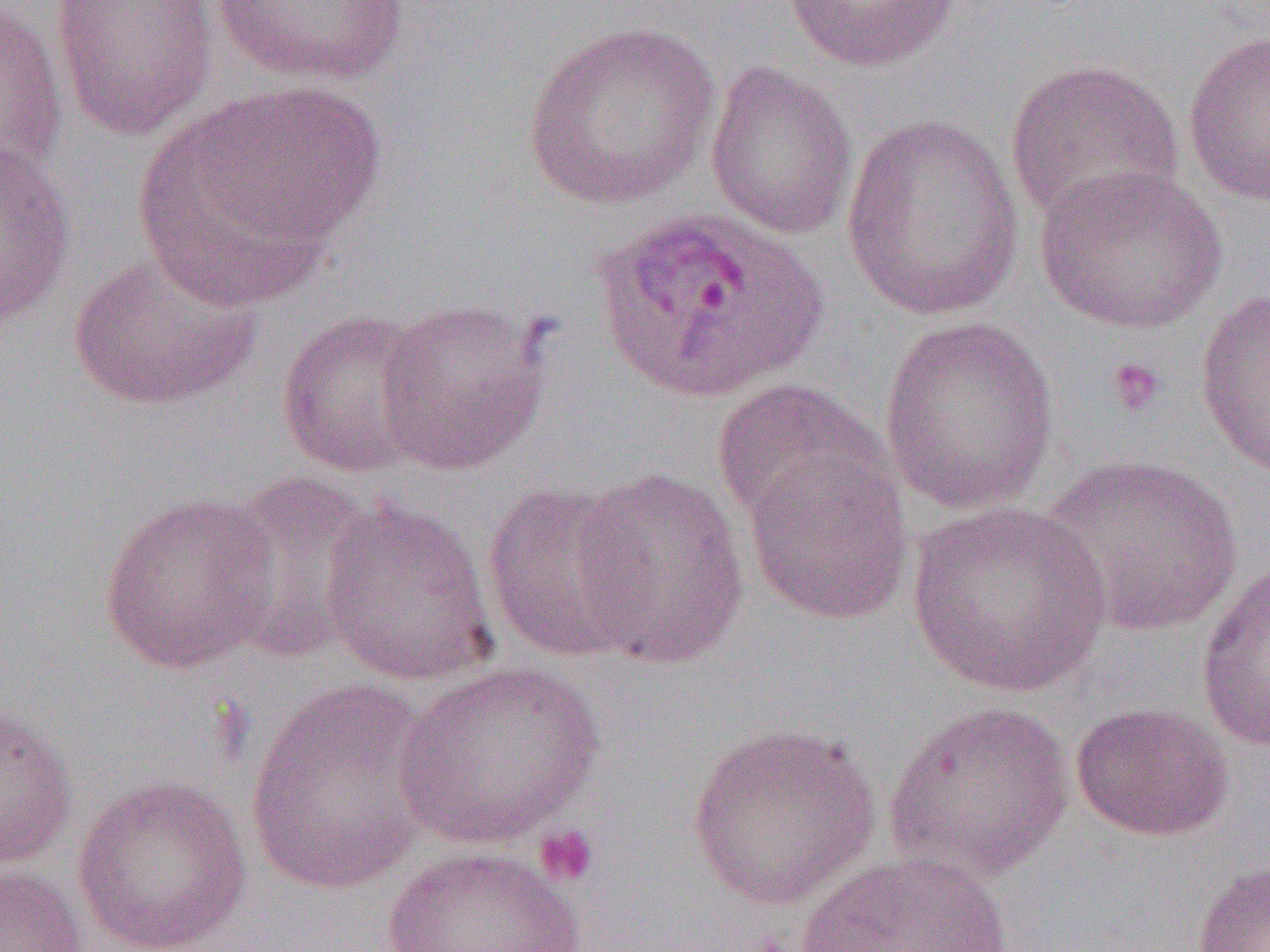

{
  "slide_level_diagnosis": "Plasmodium ovale",
  "magnification": "1000x",
  "preparation": "thin blood smear",
  "plasmodium_ovale_infected_red_blood_cell_locations": "approximate bounding boxes as (x1, y1, x2, y2) in pixels: (592, 205, 828, 405)",
  "modality": "optical microscopy",
  "image_size": "1270×952 pixels",
  "uninfected_red_blood_cell_locations": "approximate bounding boxes as (x1, y1, x2, y2) in pixels: (49, 0, 219, 141), (211, 0, 411, 87), (782, 0, 962, 72), (0, 3, 68, 184), (520, 21, 721, 211), (1183, 28, 1270, 208), (1005, 58, 1186, 230), (704, 60, 859, 241), (141, 82, 387, 288), (841, 114, 1026, 322), (0, 141, 77, 330), (1035, 163, 1229, 335), (67, 248, 266, 412), (1194, 287, 1270, 478), (374, 297, 553, 475), (275, 308, 435, 479), (877, 313, 1062, 517), (710, 379, 894, 533), (741, 445, 916, 627), (1037, 453, 1244, 639), (568, 467, 749, 668), (212, 472, 381, 664), (480, 483, 649, 664), (98, 491, 281, 675), (319, 498, 499, 686), (906, 501, 1114, 698), (1195, 561, 1270, 750), (393, 661, 605, 849), (244, 681, 440, 897), (882, 699, 1076, 886), (0, 701, 78, 870), (1070, 702, 1233, 842), (686, 721, 882, 910), (72, 774, 253, 952), (378, 846, 594, 952), (795, 851, 1016, 952), (1191, 858, 1269, 951), (0, 863, 87, 952)",
  "platelet_locations": "approximate bounding boxes as (x1, y1, x2, y2) in pixels: (1105, 356, 1167, 418), (532, 824, 601, 888)",
  "field_of_view": "one of a larger specimen"
}